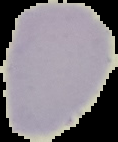

Image is 118×142 pixels. From a thin blood smear. Malaria status: uninfected. Segmented cell region on a black background.